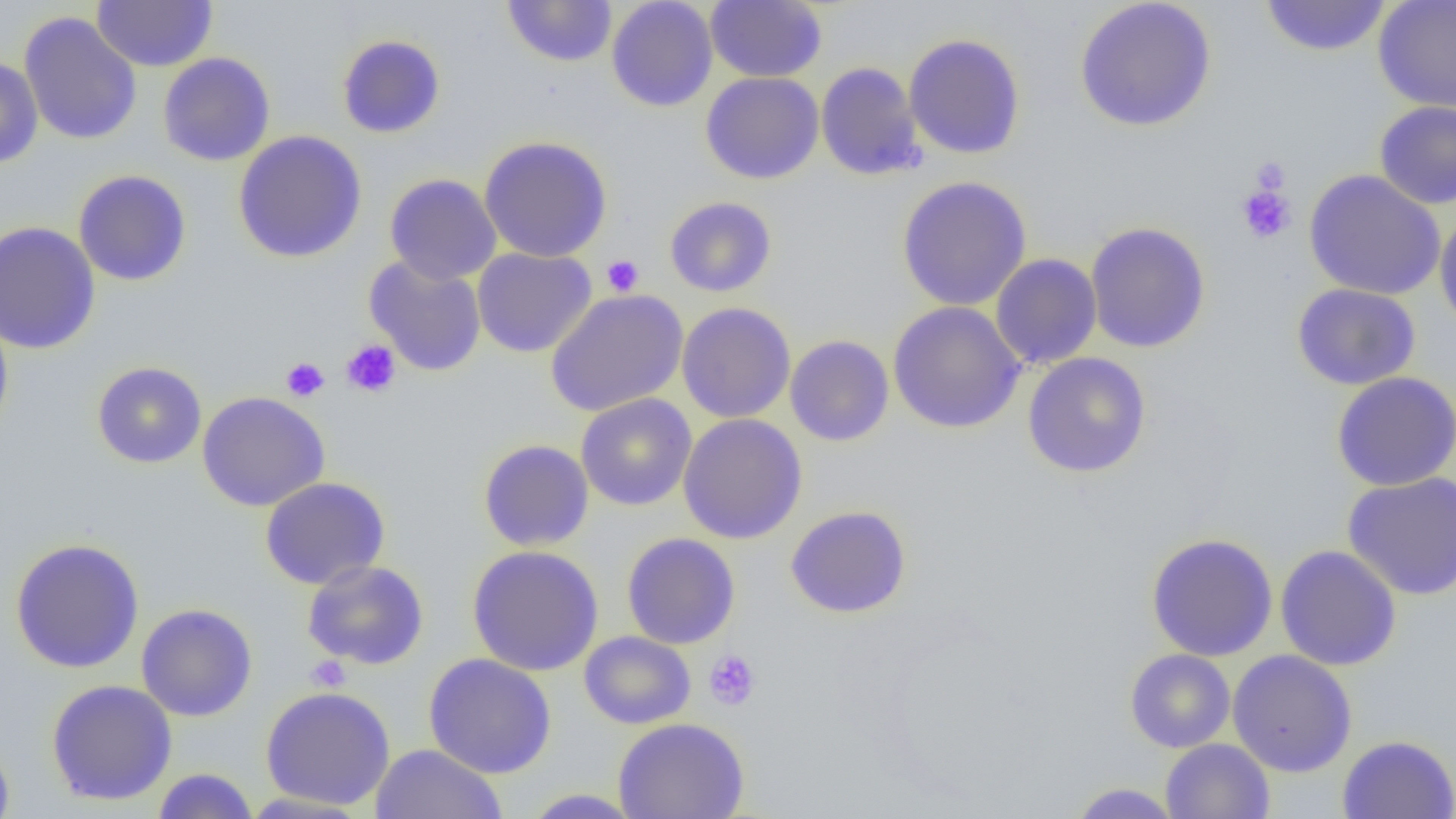 Approximate bounding boxes as [x1, y1, x2, y2] in pixels. Uninfected red blood cell locations: [92, 0, 217, 73], [502, 0, 618, 67], [606, 0, 718, 112], [705, 0, 827, 83], [1074, 0, 1217, 132], [1259, 0, 1392, 57], [1373, 0, 1456, 113], [19, 12, 142, 145], [903, 33, 1026, 160], [337, 34, 445, 138], [158, 52, 276, 167], [0, 57, 43, 168], [815, 62, 926, 181], [700, 71, 824, 184], [1374, 100, 1456, 209], [232, 130, 368, 263], [478, 136, 613, 263], [73, 170, 191, 286], [1303, 170, 1446, 300], [385, 174, 502, 285], [895, 176, 1033, 311], [664, 196, 777, 297], [1434, 210, 1456, 335], [0, 221, 100, 355], [1085, 221, 1211, 353], [472, 247, 597, 358], [990, 253, 1103, 369], [364, 255, 488, 377], [1292, 283, 1421, 390], [545, 289, 689, 416], [887, 301, 1026, 434], [676, 302, 796, 423], [0, 311, 13, 440], [785, 335, 894, 446], [1022, 352, 1151, 478], [91, 361, 207, 469], [1331, 371, 1456, 491], [197, 391, 330, 512], [575, 393, 697, 511], [678, 413, 807, 544], [478, 439, 594, 551], [1342, 471, 1456, 601], [260, 477, 390, 590], [785, 505, 912, 619], [1145, 532, 1279, 661], [621, 533, 740, 649], [9, 538, 145, 674], [1275, 544, 1402, 671], [467, 545, 604, 676], [302, 560, 429, 670], [136, 603, 258, 722], [579, 631, 696, 729], [1124, 649, 1236, 753], [1227, 650, 1357, 777], [423, 653, 556, 778], [46, 679, 178, 805], [260, 686, 395, 810], [613, 717, 749, 819], [0, 735, 15, 819], [1337, 735, 1456, 819], [1161, 739, 1274, 819], [370, 744, 508, 818], [152, 768, 259, 819], [1068, 782, 1183, 818], [521, 788, 645, 818], [239, 791, 373, 818]. Platelet locations: [1248, 157, 1290, 196], [1236, 185, 1297, 244], [601, 254, 644, 296], [341, 340, 402, 397], [281, 357, 329, 402], [703, 649, 761, 711], [305, 655, 351, 692]. Slide-level diagnosis: no evidence of blood parasites. Light microscopy. 1000x magnification. Thin blood film. Image is 1456×819 pixels. Single field of view.